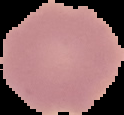

malaria status = uninfected
preparation = thin blood smear
image size = 124×115 pixels
image type = cell region segmented out of the field of view; surrounding area masked to black